Outline platelets.
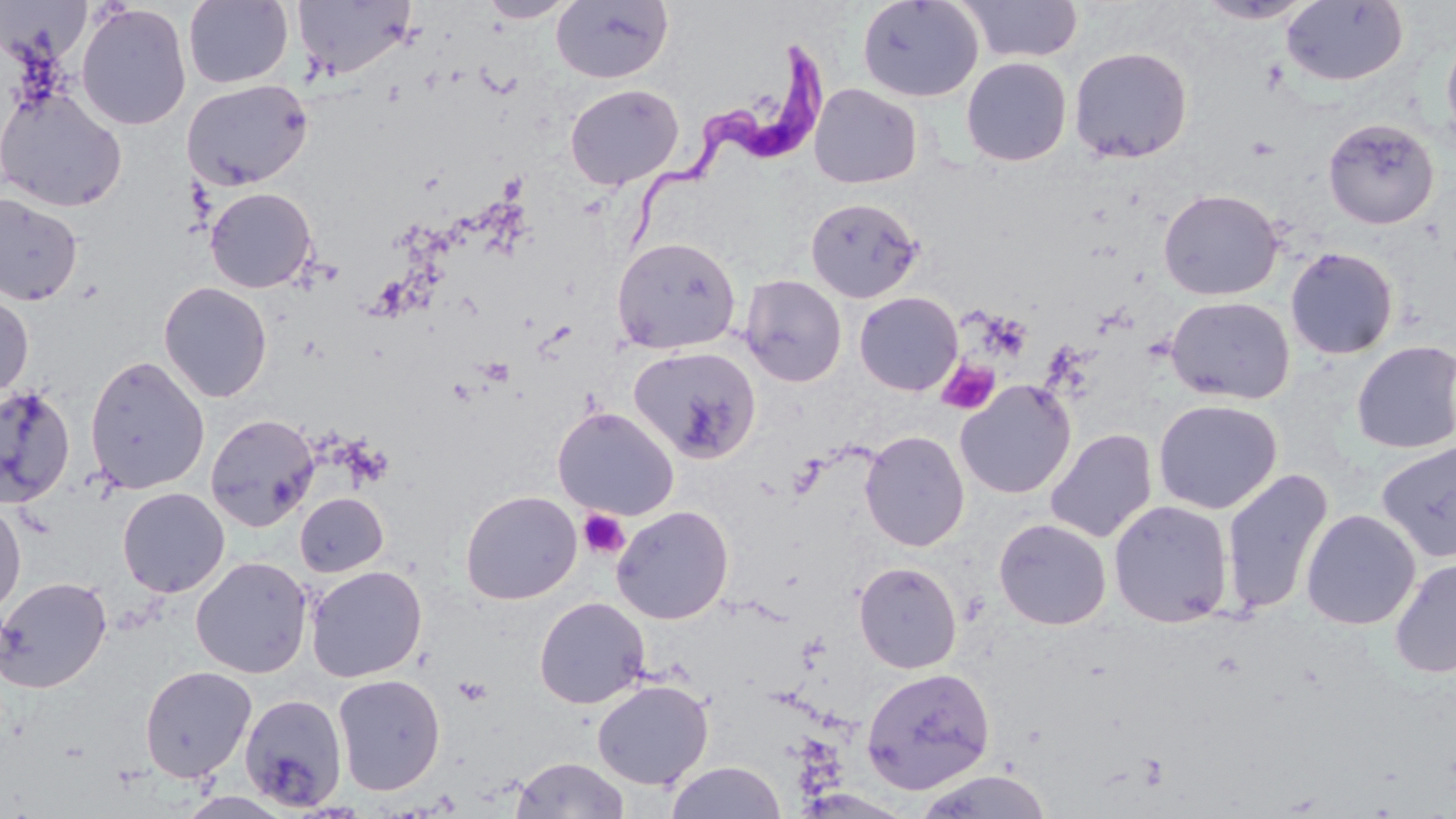

Approximate bounding boxes as named x1/y1/x2/y2 corners in pixels.
Platelets: (x1=937, y1=360, x2=1000, y2=414), (x1=577, y1=509, x2=631, y2=560), (x1=453, y1=676, x2=493, y2=706).

slide-level diagnosis = Trypanosoma brucei
modality = light microscopy
stain = May-Grünwald-Giemsa
Trypanosoma brucei locations = approximate bounding boxes as named x1/y1/x2/y2 corners in pixels: (x1=618, y1=39, x2=831, y2=261)
field of view = single
image size = 1456×819 pixels
preparation = thin blood smear
uninfected red blood cell locations = approximate bounding boxes as named x1/y1/x2/y2 corners in pixels: (x1=182, y1=0, x2=294, y2=89), (x1=478, y1=0, x2=577, y2=23), (x1=551, y1=0, x2=674, y2=84), (x1=857, y1=0, x2=983, y2=103), (x1=957, y1=0, x2=1084, y2=63), (x1=1196, y1=0, x2=1317, y2=24), (x1=292, y1=1, x2=416, y2=80), (x1=1281, y1=1, x2=1408, y2=87), (x1=1, y1=3, x2=92, y2=68), (x1=75, y1=4, x2=192, y2=130), (x1=1441, y1=30, x2=1456, y2=155), (x1=1069, y1=46, x2=1193, y2=163), (x1=961, y1=57, x2=1071, y2=166), (x1=182, y1=78, x2=313, y2=191), (x1=564, y1=83, x2=684, y2=189), (x1=809, y1=84, x2=922, y2=188), (x1=1, y1=87, x2=127, y2=212), (x1=1323, y1=117, x2=1439, y2=229), (x1=204, y1=187, x2=318, y2=293), (x1=1158, y1=189, x2=1282, y2=300), (x1=0, y1=193, x2=83, y2=307), (x1=806, y1=197, x2=924, y2=304), (x1=612, y1=236, x2=741, y2=355), (x1=1285, y1=247, x2=1399, y2=360), (x1=740, y1=274, x2=847, y2=387), (x1=158, y1=281, x2=272, y2=402), (x1=0, y1=292, x2=34, y2=399), (x1=854, y1=292, x2=963, y2=396), (x1=1166, y1=295, x2=1295, y2=405), (x1=1351, y1=340, x2=1456, y2=454), (x1=628, y1=345, x2=762, y2=464), (x1=84, y1=354, x2=210, y2=495), (x1=955, y1=380, x2=1075, y2=499), (x1=0, y1=384, x2=77, y2=510), (x1=1153, y1=399, x2=1282, y2=514), (x1=553, y1=407, x2=678, y2=520), (x1=206, y1=413, x2=318, y2=531), (x1=1045, y1=428, x2=1157, y2=543), (x1=860, y1=430, x2=970, y2=552), (x1=1376, y1=440, x2=1456, y2=562), (x1=1221, y1=468, x2=1333, y2=617), (x1=117, y1=487, x2=229, y2=598), (x1=460, y1=490, x2=582, y2=605), (x1=295, y1=493, x2=388, y2=577), (x1=0, y1=499, x2=26, y2=617), (x1=1108, y1=499, x2=1234, y2=628), (x1=611, y1=505, x2=734, y2=624), (x1=1301, y1=509, x2=1421, y2=630), (x1=994, y1=518, x2=1111, y2=630), (x1=191, y1=556, x2=312, y2=678), (x1=1389, y1=557, x2=1456, y2=679), (x1=854, y1=561, x2=962, y2=674), (x1=306, y1=565, x2=428, y2=682), (x1=0, y1=575, x2=112, y2=693), (x1=534, y1=596, x2=650, y2=709), (x1=139, y1=665, x2=257, y2=782), (x1=861, y1=667, x2=996, y2=794), (x1=331, y1=673, x2=446, y2=796), (x1=592, y1=679, x2=713, y2=790), (x1=239, y1=692, x2=348, y2=812), (x1=512, y1=756, x2=629, y2=818), (x1=665, y1=761, x2=786, y2=819), (x1=914, y1=770, x2=1053, y2=819)
magnification = 1000x